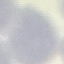

Result: no malaria parasites detected. Giemsa stain. Thin blood smear. Automatically extracted cell patch, resized to 64 × 64 pixels. Acquired by smartphone through the microscope eyepiece.